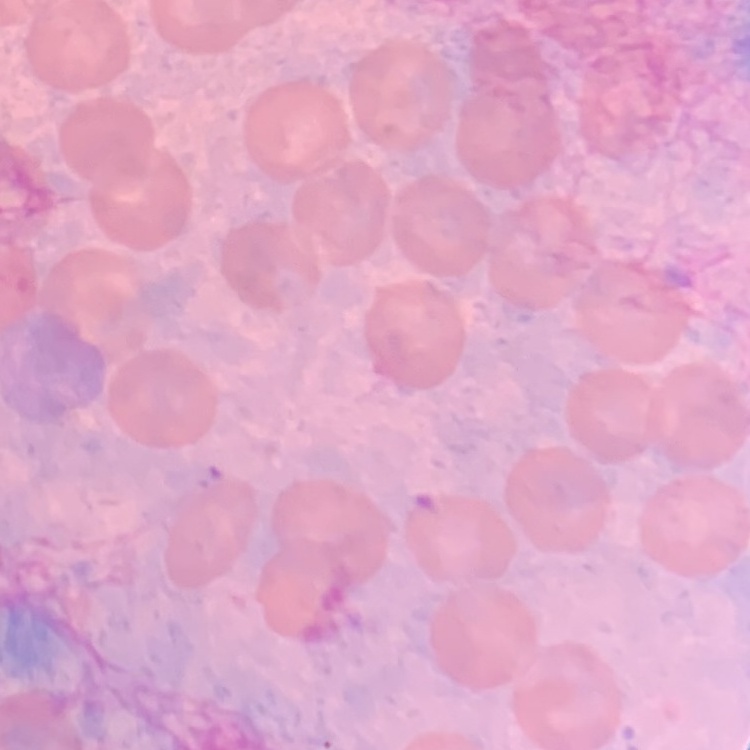 The erythrocytes exhibit no rouleaux formation. Square crop of a larger photomicrograph. Field's or Giemsa stain. Thin peripheral smear.